Outline each blood parasite and name the species.
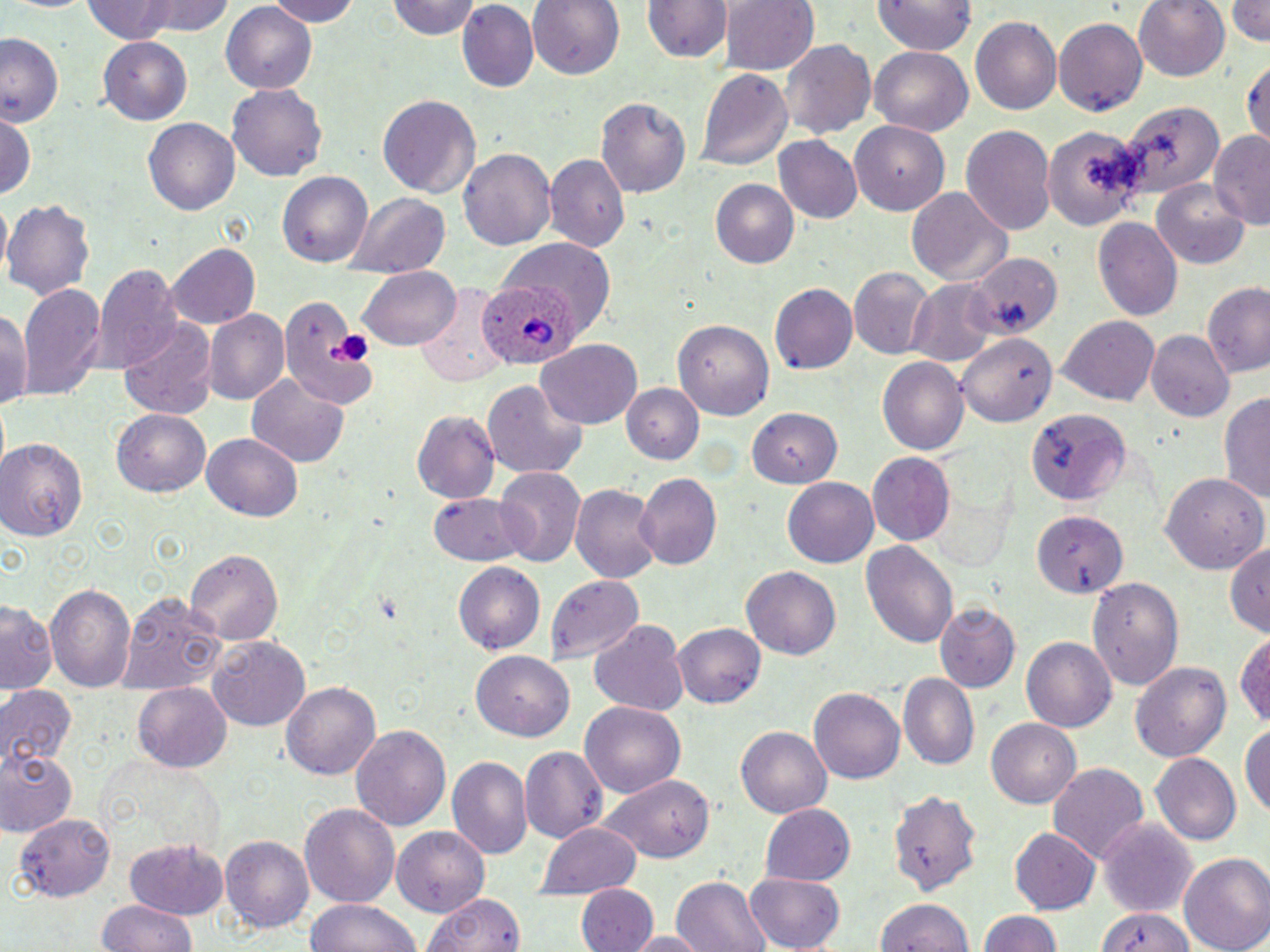
Approximate bounding boxes as [x1, y1, x2, y2] in pixels.
Plasmodium ovale-infected red blood cells: [479, 282, 580, 369].
No Plasmodium falciparum, Plasmodium malariae, Plasmodium vivax, Babesia divergens, or Trypanosoma brucei observed.

slide_level_diagnosis: Plasmodium ovale
magnification: 1000x
preparation: thin blood smear
field_of_view: single
platelet_locations: 'approximate bounding boxes as [x1, y1, x2, y2] in pixels: [326, 332, 369, 364]'
modality: light microscopy
uninfected_red_blood_cell_locations: 'approximate bounding boxes as [x1, y1, x2, y2] in pixels: [80, 0, 221, 43], [259, 0, 365, 26], [389, 0, 484, 41], [527, 0, 625, 80], [722, 0, 819, 76], [1133, 0, 1230, 81], [1229, 0, 1270, 47], [644, 1, 729, 65], [873, 1, 976, 56], [456, 3, 539, 92], [220, 5, 319, 93], [969, 15, 1063, 116], [1054, 18, 1148, 116], [0, 34, 65, 128], [98, 38, 192, 123], [783, 40, 876, 141], [868, 46, 973, 137], [1244, 59, 1270, 150], [696, 65, 792, 173], [228, 84, 327, 181], [377, 95, 480, 199], [595, 96, 691, 199], [1116, 99, 1225, 197], [2, 112, 37, 206], [144, 117, 242, 215], [850, 120, 950, 212], [961, 124, 1056, 237], [1044, 124, 1143, 230], [1211, 132, 1270, 227], [773, 136, 862, 224], [458, 148, 558, 252], [545, 154, 627, 251], [279, 171, 372, 268], [1152, 178, 1250, 268], [708, 179, 799, 267], [907, 188, 1009, 287], [345, 194, 449, 276], [3, 198, 95, 299], [1092, 218, 1182, 322], [505, 238, 619, 302], [167, 242, 260, 330], [967, 253, 1060, 341], [359, 264, 461, 349], [95, 265, 182, 370], [848, 266, 936, 359], [907, 279, 1000, 366], [1202, 283, 1270, 376], [770, 284, 858, 375], [18, 285, 105, 400], [280, 293, 372, 411], [0, 304, 33, 412], [204, 310, 290, 407], [117, 315, 216, 417], [1057, 316, 1162, 406], [675, 318, 774, 420], [1149, 329, 1235, 421], [959, 334, 1057, 426], [537, 340, 642, 428], [878, 357, 970, 454], [248, 375, 351, 467], [480, 379, 588, 478], [622, 384, 703, 464], [1218, 389, 1270, 509], [1020, 405, 1133, 507], [747, 407, 844, 488], [112, 408, 211, 498], [412, 412, 499, 504], [202, 431, 303, 522], [0, 438, 87, 542], [869, 452, 953, 542], [498, 467, 585, 565], [633, 472, 720, 569], [1159, 472, 1265, 575], [783, 475, 880, 565], [572, 483, 662, 585], [429, 491, 528, 566], [1034, 510, 1128, 598], [1227, 537, 1269, 637], [863, 540, 958, 650], [184, 548, 282, 642], [455, 562, 545, 656], [741, 566, 842, 660], [546, 573, 642, 659], [1087, 576, 1182, 687], [43, 580, 137, 692], [122, 592, 228, 694], [1, 601, 56, 693], [933, 603, 1020, 693], [589, 619, 690, 716], [674, 623, 766, 708], [1235, 627, 1269, 728], [1022, 636, 1116, 731], [208, 637, 310, 730], [471, 651, 575, 740], [1130, 661, 1233, 765], [901, 675, 979, 768], [283, 682, 381, 781], [135, 683, 231, 773], [0, 685, 77, 774], [810, 686, 908, 784], [578, 702, 685, 797], [987, 718, 1081, 805], [1243, 721, 1270, 818], [354, 724, 450, 830], [737, 726, 831, 818], [519, 745, 609, 844], [0, 748, 76, 834], [1152, 755, 1241, 846], [447, 756, 531, 857], [1049, 762, 1148, 865], [599, 773, 714, 862], [886, 785, 982, 897], [298, 802, 400, 909], [760, 802, 855, 886], [19, 813, 115, 901], [1099, 818, 1199, 920], [536, 822, 644, 897], [392, 827, 488, 911], [1010, 830, 1100, 914], [124, 836, 230, 920], [221, 836, 315, 932], [1179, 851, 1270, 952], [743, 872, 847, 951], [672, 875, 769, 952], [577, 885, 658, 952], [421, 891, 527, 952], [307, 898, 422, 952], [875, 899, 978, 952], [96, 901, 203, 952], [1095, 905, 1197, 952], [975, 909, 1066, 952], [1096, 909, 1201, 952], [630, 932, 702, 952]'
image_size: 1270×952 pixels
stain: May-Grünwald-Giemsa